Name the parasite shown.
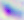

Toxoplasma gondii.

{
  "modality": "photomicrograph",
  "magnification": "400x"
}